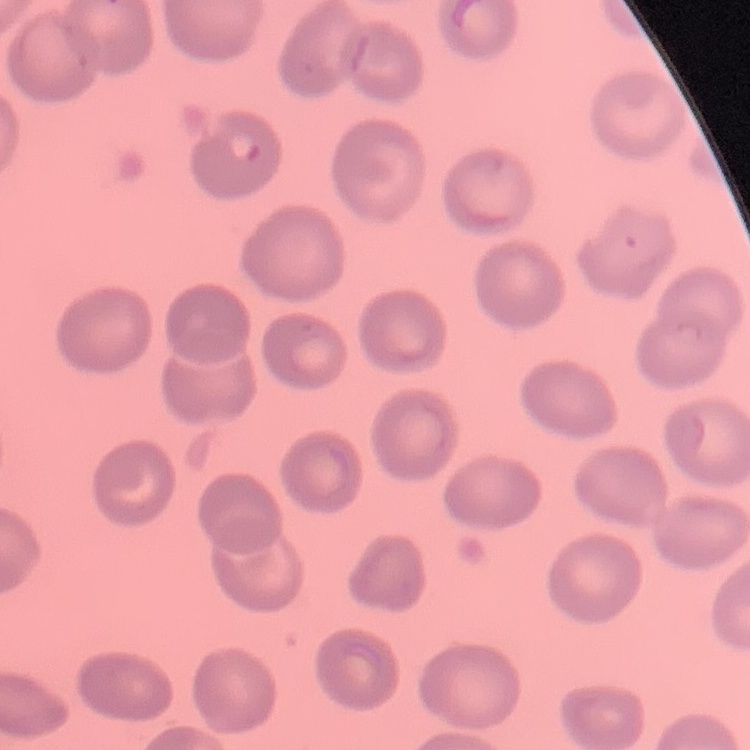

Summary:
  - Erythrocyte morphology: no rouleaux formation
  - Image type: one tile cut from a larger photomicrograph
  - Preparation: thin blood smear
  - Stain: Field's or Giemsa